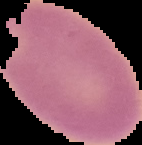

image_size: 142×145 pixels
malaria_status: uninfected
image_type: segmented cell region with the area outside set to black
preparation: thin blood smear